State the blood parasite species.
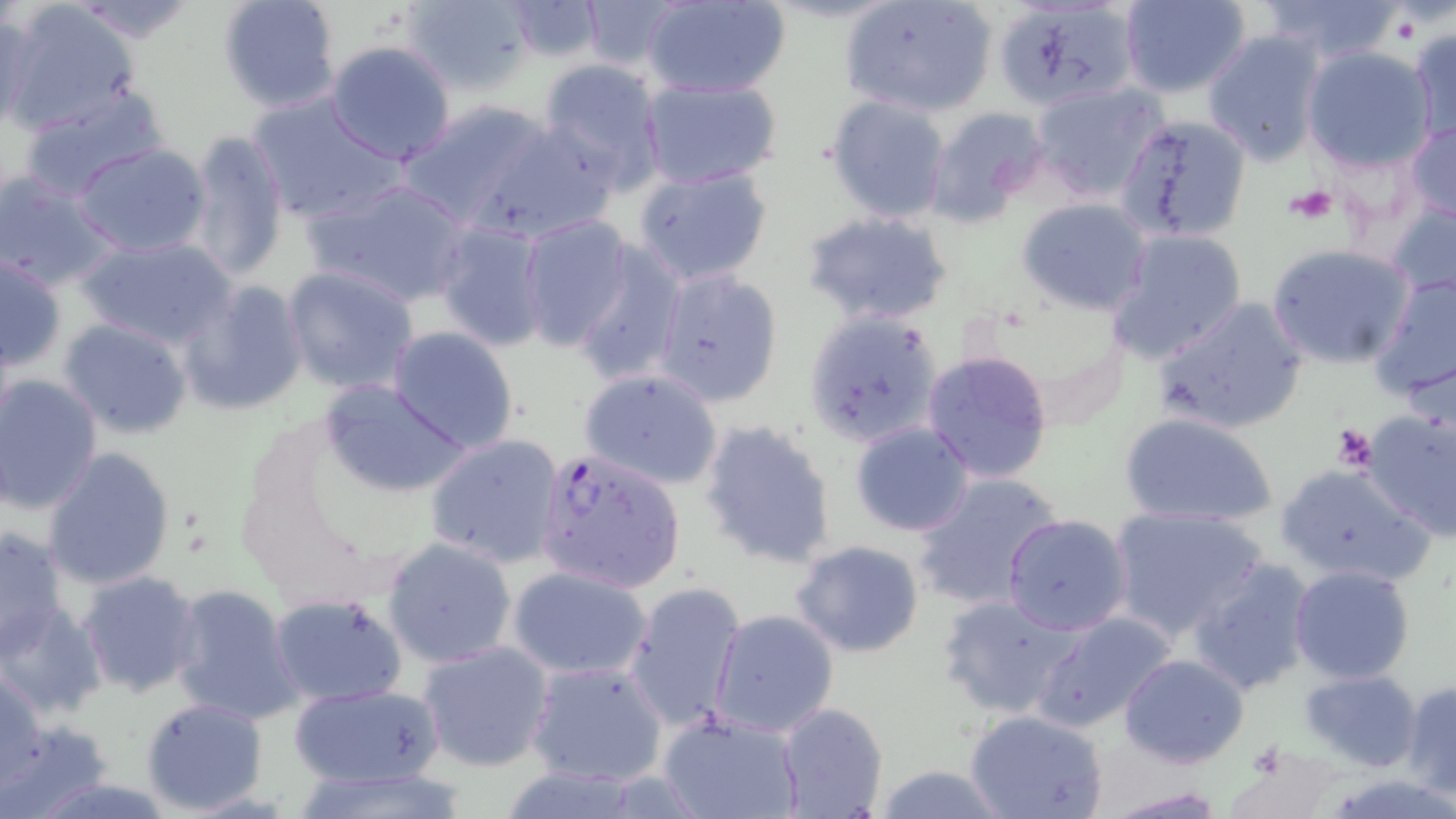

Plasmodium falciparum.

Summary:
  - Coordinate format: approximate bounding boxes as [x1, y1, x2, y2] in pixels
  - Platelet locations: [1286, 184, 1338, 225], [1331, 424, 1377, 472]
  - Uninfected red blood cell locations: [215, 0, 342, 114], [399, 0, 535, 97], [501, 0, 607, 63], [578, 0, 686, 74], [643, 0, 790, 99], [840, 0, 998, 118], [1119, 0, 1251, 98], [1262, 0, 1405, 67], [67, 2, 202, 45], [1, 3, 143, 135], [997, 4, 1219, 116], [0, 7, 39, 130], [1405, 28, 1455, 143], [1202, 30, 1325, 166], [1002, 33, 1152, 156], [324, 41, 458, 165], [1301, 46, 1437, 172], [537, 59, 667, 187], [637, 75, 781, 187], [1030, 81, 1167, 202], [17, 85, 171, 201], [246, 90, 405, 225], [825, 94, 953, 223], [400, 100, 559, 228], [921, 104, 1050, 225], [207, 106, 354, 260], [1117, 115, 1251, 242], [471, 117, 622, 240], [1406, 119, 1456, 224], [183, 130, 291, 285], [73, 144, 214, 259], [632, 162, 775, 286], [0, 170, 118, 292], [304, 176, 473, 308], [1016, 196, 1151, 316], [1386, 201, 1456, 302], [801, 210, 954, 329], [517, 215, 635, 350], [433, 220, 552, 353], [1104, 229, 1248, 365], [77, 235, 236, 350], [571, 242, 685, 386], [1265, 243, 1416, 371], [1, 252, 69, 373], [281, 265, 419, 396], [650, 266, 784, 409], [1370, 270, 1456, 404], [178, 281, 307, 416], [1153, 296, 1308, 436], [803, 310, 940, 449], [58, 318, 193, 440], [388, 327, 519, 454], [921, 349, 1055, 485], [578, 369, 724, 491], [0, 374, 103, 515], [317, 382, 470, 500], [1357, 406, 1456, 540], [1118, 410, 1280, 529], [697, 418, 839, 569], [848, 419, 976, 537], [425, 434, 566, 568], [40, 449, 177, 590], [1273, 460, 1433, 588], [910, 468, 1064, 612], [1108, 506, 1269, 640], [1002, 514, 1132, 636], [0, 526, 70, 665], [382, 537, 518, 669], [790, 540, 926, 658], [1185, 558, 1316, 696], [506, 564, 654, 680], [1288, 564, 1417, 683], [76, 570, 203, 698], [623, 580, 747, 734], [168, 584, 302, 726], [269, 592, 407, 706], [936, 593, 1084, 720], [1, 601, 104, 721], [710, 608, 840, 736], [1031, 611, 1177, 734], [416, 639, 556, 771], [1120, 654, 1249, 769], [525, 658, 669, 788], [1, 666, 47, 796], [1300, 669, 1422, 771], [1401, 681, 1456, 801], [287, 682, 448, 792], [139, 697, 269, 814], [776, 702, 889, 819], [966, 710, 1109, 819], [660, 712, 806, 819], [4, 716, 114, 813], [1225, 743, 1341, 818], [869, 764, 1013, 819], [1098, 787, 1230, 818]
  - Plasmodium falciparum-infected red blood cell locations: [534, 448, 686, 594]
  - Preparation: thin blood smear
  - Modality: optical microscopy
  - Field of view: one of a larger specimen
  - Magnification: 1000x
  - Stain: May-Grünwald-Giemsa
  - Image size: 1456×819 pixels